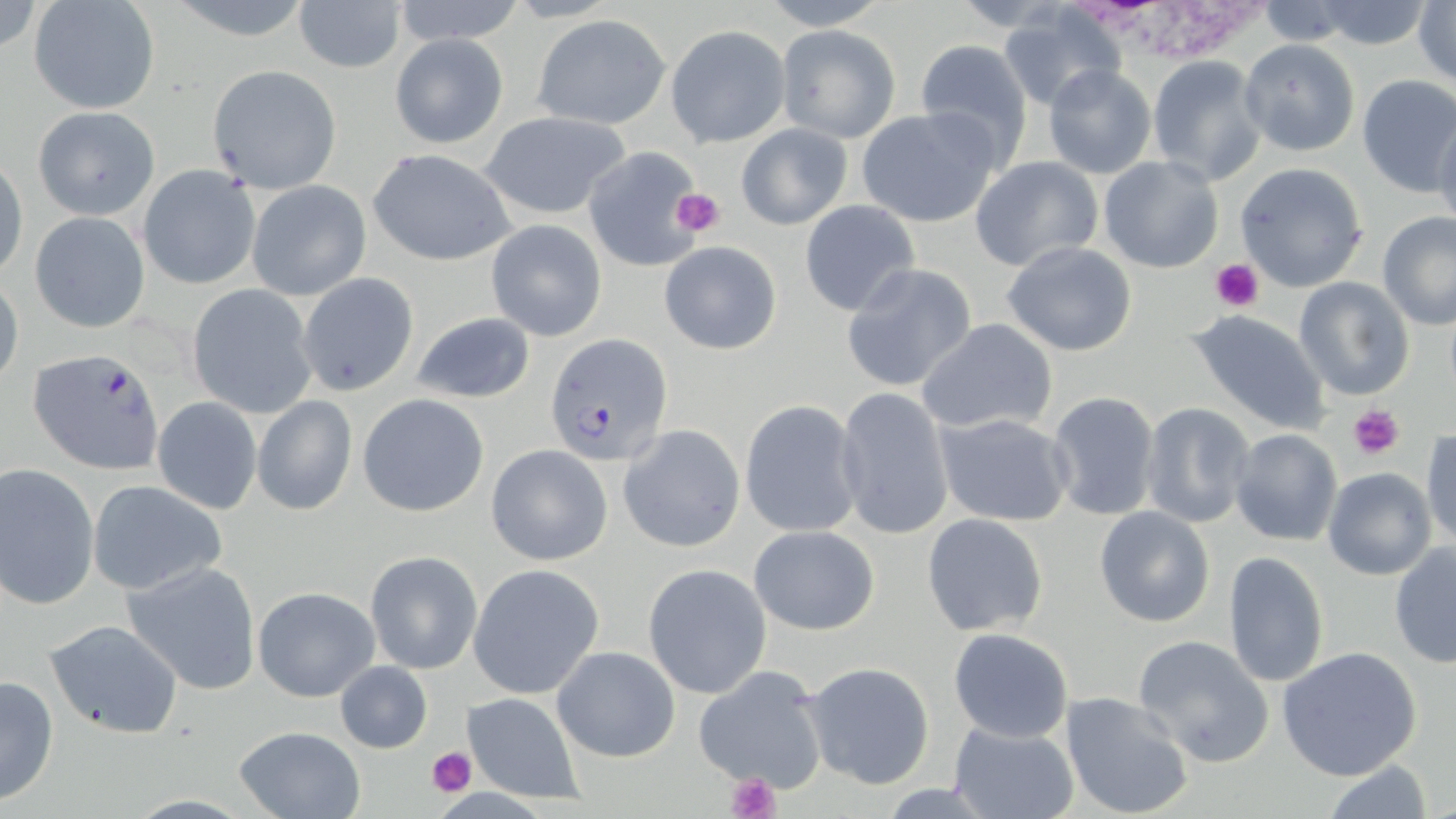
Approximate bounding boxes as (x1, y1, x2, y2) in pixels. Plasmodium falciparum-infected red blood cell locations: (545, 334, 673, 468), (28, 348, 167, 474). Platelet locations: (671, 189, 724, 237), (1210, 258, 1264, 311), (1349, 406, 1405, 460), (427, 745, 476, 797), (722, 774, 780, 819). White blood cell locations: (1079, 1, 1267, 66). Uninfected red blood cell locations: (391, 0, 529, 48), (293, 1, 406, 75), (751, 1, 898, 29), (1302, 1, 1440, 49), (1414, 2, 1455, 90), (30, 3, 159, 114), (1255, 3, 1361, 44), (996, 7, 1127, 111), (531, 14, 671, 129), (777, 23, 899, 143), (664, 24, 791, 148), (389, 32, 508, 149), (913, 39, 1034, 167), (1239, 39, 1361, 156), (1145, 55, 1268, 186), (208, 64, 342, 192), (1042, 64, 1158, 180), (1355, 75, 1456, 196), (32, 106, 160, 220), (856, 106, 1002, 229), (477, 110, 635, 220), (1432, 113, 1456, 235), (735, 123, 852, 230), (583, 143, 705, 272), (368, 148, 518, 266), (1097, 156, 1224, 273), (970, 157, 1105, 273), (1, 158, 27, 280), (1234, 161, 1369, 294), (139, 165, 261, 288), (247, 180, 370, 301), (799, 199, 920, 315), (29, 210, 153, 334), (1376, 211, 1456, 329), (486, 220, 607, 341), (659, 240, 782, 354), (1001, 240, 1138, 357), (840, 262, 981, 394), (297, 273, 419, 395), (1293, 275, 1416, 402), (0, 276, 24, 393), (186, 286, 318, 418), (409, 310, 538, 405), (1187, 310, 1331, 433), (916, 318, 1063, 438), (833, 386, 955, 540), (1046, 389, 1162, 520), (358, 393, 491, 517), (252, 395, 357, 514), (152, 397, 262, 515), (739, 398, 863, 538), (1138, 402, 1256, 528), (935, 412, 1075, 527), (617, 424, 745, 552), (1228, 429, 1344, 547), (1421, 429, 1455, 548), (485, 444, 613, 566), (0, 463, 100, 610), (1323, 466, 1437, 580), (1264, 478, 1372, 628), (86, 481, 226, 597), (1094, 506, 1215, 627), (921, 513, 1049, 637), (748, 525, 879, 635), (1389, 541, 1455, 669), (364, 550, 483, 675), (1224, 550, 1331, 690), (121, 560, 263, 695), (468, 563, 605, 699), (643, 563, 772, 699), (252, 586, 378, 702), (45, 619, 183, 740), (948, 627, 1075, 743), (1132, 635, 1277, 768), (552, 645, 681, 762), (1276, 646, 1424, 780), (334, 660, 433, 753), (800, 661, 937, 790), (692, 662, 831, 793), (0, 674, 60, 806), (461, 691, 585, 804), (1059, 691, 1196, 819), (947, 720, 1080, 819), (232, 725, 367, 818), (1321, 760, 1438, 817). Slide-level diagnosis: Plasmodium falciparum. Image is 1456×819 pixels. Captured at 1000x magnification. Thin blood smear. May-Grünwald-Giemsa stain. Light microscopy. Single field of view.